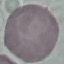
Summary:
  - Malaria status: uninfected
  - Preparation: thin blood film
  - Stain: Giemsa
  - Capture: smartphone through the microscope eyepiece
  - Image type: cell patch, automatically extracted from a larger field of view and resized to 64 × 64 pixels